Assess this cell for malaria.
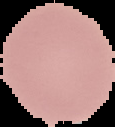

Uninfected.

Image is 115×127 pixels. From a thin blood film. Cell region segmented out of the field of view; the surrounding area is masked to black.